Identify the parasite.
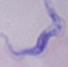

This is a trypanosome.

Micrograph. 1000x magnification.